Locate and identify every blood parasite.
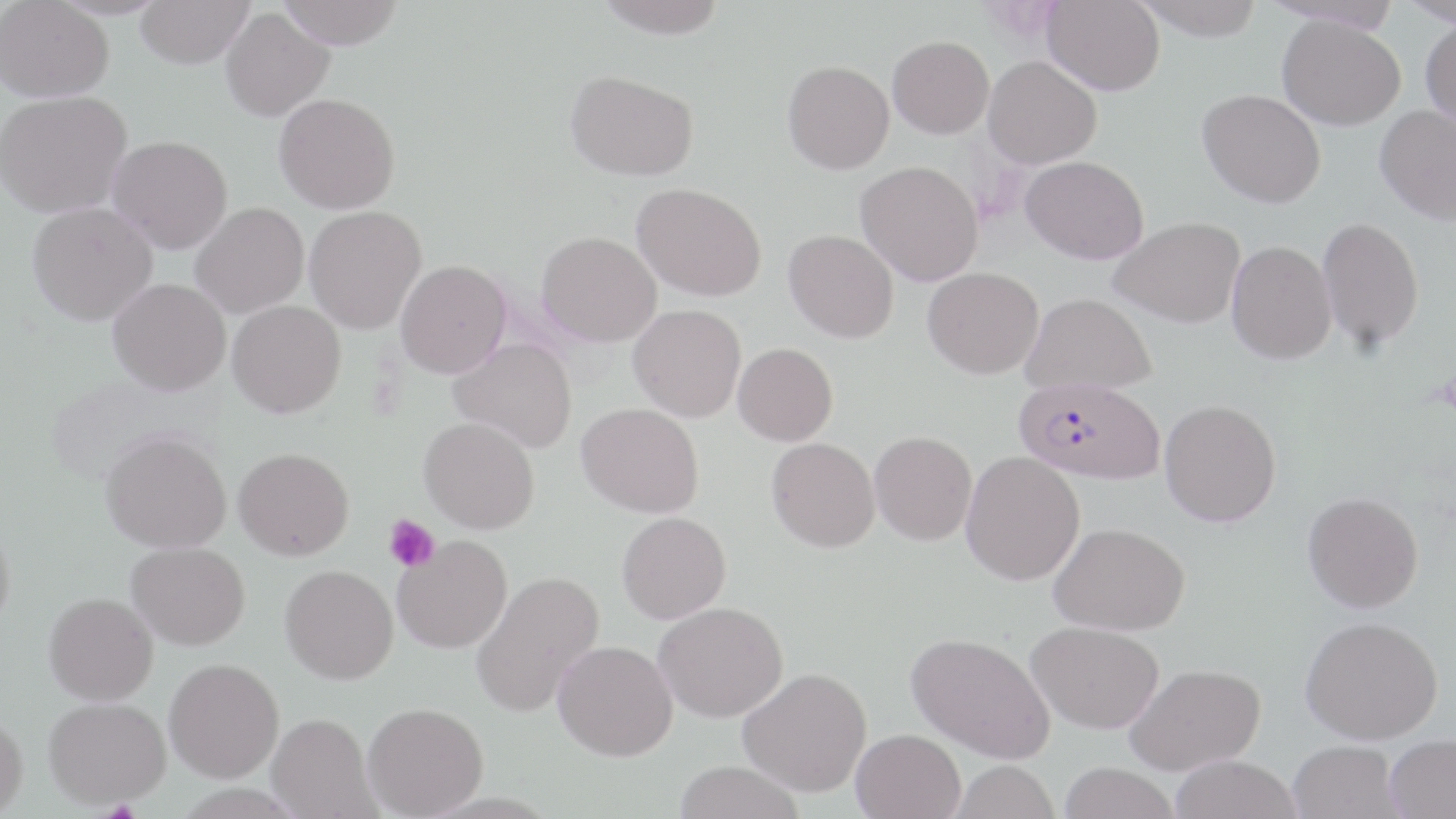

Approximate bounding boxes as [x1, y1, x2, y2] in pixels.
Plasmodium falciparum-infected red blood cells: [1014, 377, 1165, 484].
No Plasmodium ovale, Plasmodium malariae, Plasmodium vivax, Babesia divergens, or Trypanosoma brucei observed.

Summary:
  - Uninfected red blood cell locations: [137, 0, 252, 69], [278, 0, 404, 49], [594, 0, 727, 39], [1043, 0, 1165, 96], [1134, 0, 1266, 41], [1398, 0, 1456, 27], [0, 1, 114, 103], [1267, 2, 1405, 34], [220, 7, 335, 122], [1277, 15, 1406, 130], [1420, 17, 1456, 128], [887, 36, 994, 138], [984, 55, 1102, 168], [782, 60, 894, 174], [565, 69, 699, 181], [1198, 88, 1326, 208], [0, 91, 132, 218], [274, 93, 400, 214], [1375, 104, 1456, 225], [107, 135, 233, 254], [1021, 155, 1149, 264], [856, 161, 983, 286], [632, 183, 766, 301], [27, 202, 158, 326], [190, 202, 309, 318], [303, 206, 427, 334], [1110, 216, 1245, 328], [1317, 216, 1425, 351], [783, 229, 899, 343], [537, 231, 661, 346], [1226, 240, 1336, 364], [395, 259, 511, 378], [923, 267, 1044, 378], [108, 278, 232, 396], [1021, 292, 1157, 394], [227, 300, 346, 418], [628, 304, 746, 422], [449, 338, 577, 453], [733, 343, 837, 446], [1159, 399, 1282, 526], [577, 402, 704, 518], [419, 417, 539, 534], [101, 430, 232, 553], [869, 430, 977, 545], [767, 437, 880, 552], [233, 447, 354, 560], [961, 452, 1085, 585], [1302, 492, 1424, 612], [617, 511, 731, 624], [0, 517, 15, 635], [1049, 522, 1190, 635], [392, 535, 512, 654], [126, 542, 250, 650], [280, 565, 398, 684], [470, 570, 606, 717], [44, 592, 158, 705], [653, 601, 788, 722], [1300, 615, 1443, 744], [1026, 620, 1164, 734], [905, 631, 1056, 763], [552, 640, 677, 761], [164, 658, 284, 783], [1125, 663, 1266, 775], [738, 666, 873, 798], [43, 696, 170, 808], [362, 702, 488, 818], [0, 713, 28, 817], [266, 713, 380, 819], [851, 729, 966, 818], [1384, 734, 1456, 818], [1288, 740, 1404, 819], [1169, 756, 1302, 819], [673, 760, 804, 819], [949, 761, 1060, 819], [1058, 762, 1180, 819]
  - Platelet locations: [383, 514, 440, 574]
  - Slide-level diagnosis: Plasmodium falciparum
  - Stain: May-Grünwald-Giemsa
  - Image size: 1456×819 pixels
  - Field of view: one of a larger specimen
  - Modality: light microscopy
  - Magnification: 1000x
  - Preparation: thin blood smear